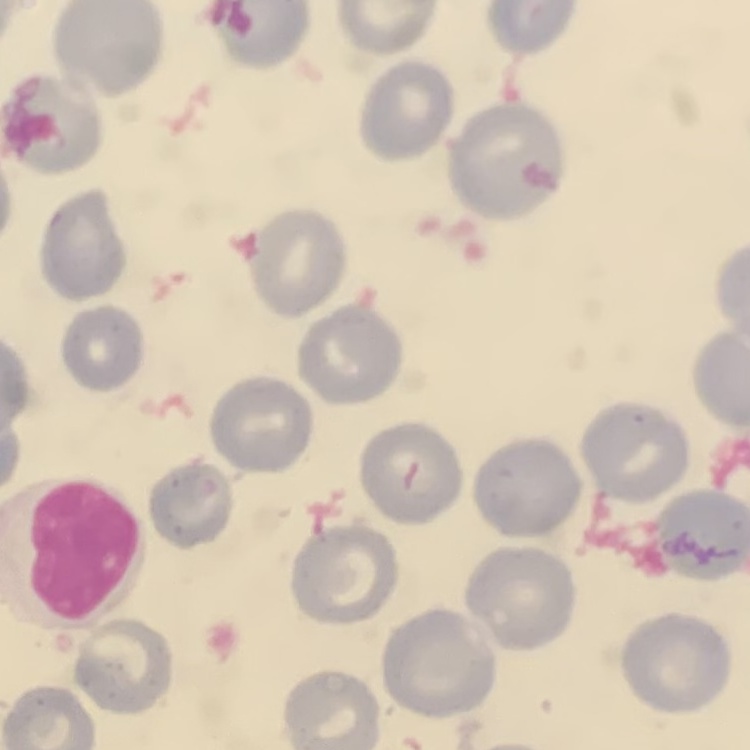

red blood cell morphology = no rouleaux formation
preparation = thin blood film
image type = one tile cut from a larger photomicrograph
stain = Field's or Giemsa